Report the malaria status of this cell.
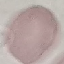
Uninfected.

{
  "preparation": "thin blood film",
  "capture": "smartphone through the microscope eyepiece",
  "stain": "Giemsa",
  "image_type": "automatically extracted cell patch, resized to 64 × 64 pixels"
}